Comment on the morphology of the erythrocytes.
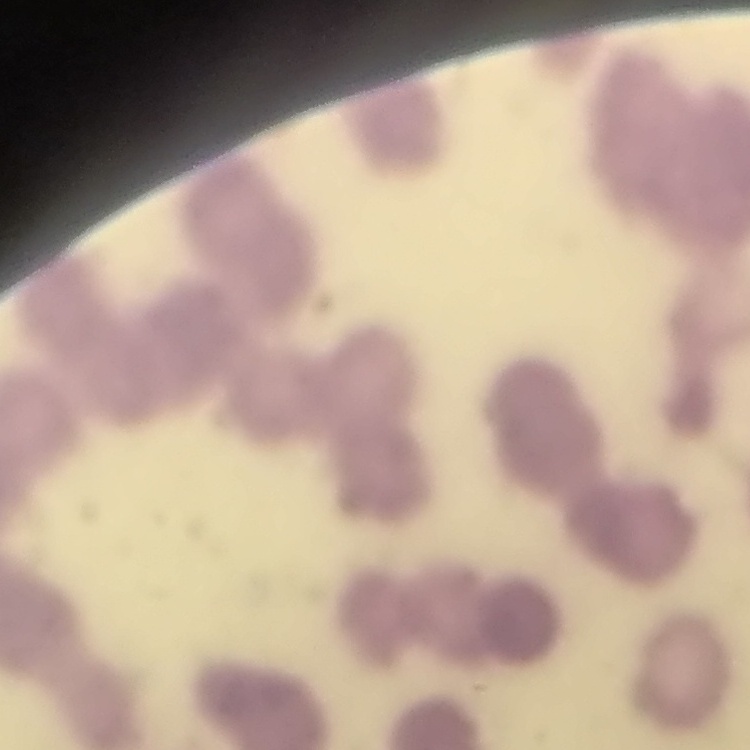
Rouleaux formation.

preparation: thin peripheral smear
image_type: one tile cut from a larger photomicrograph
stain: Field's or Giemsa